Name the blood parasite species.
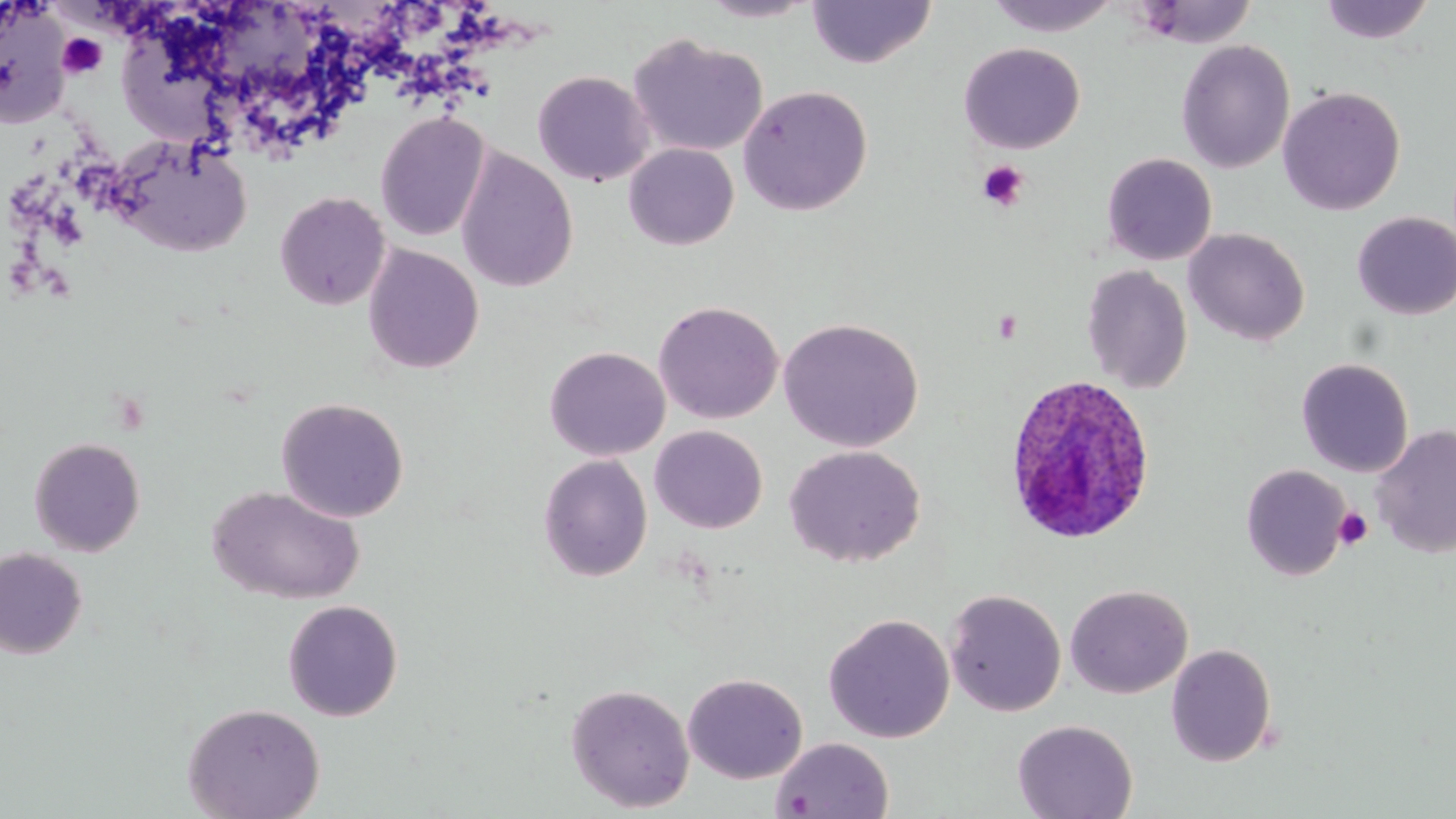
Plasmodium ovale.

Summary:
  - Coordinate format: approximate bounding boxes as (x1,y1)-(x2,y2) corner pairs in pixels
  - Plasmodium ovale-infected red blood cell locations: (1000,374)-(1155,547)
  - Platelet locations: (57,33)-(106,78), (977,160)-(1028,211), (1333,507)-(1373,550)
  - Uninfected red blood cell locations: (696,0)-(823,23), (1317,0)-(1438,45), (0,1)-(72,127), (806,1)-(937,69), (983,1)-(1123,37), (1130,1)-(1258,48), (628,33)-(768,158), (1175,40)-(1295,174), (958,42)-(1085,154), (532,70)-(654,187), (737,84)-(873,215), (1277,86)-(1406,216), (374,111)-(491,242), (106,134)-(254,257), (624,144)-(739,250), (455,147)-(578,294), (1101,153)-(1218,265), (275,191)-(391,311), (1352,212)-(1456,320), (1184,228)-(1310,346), (362,244)-(484,375), (1081,265)-(1193,393), (654,300)-(784,424), (778,317)-(924,452), (544,346)-(670,461), (1296,357)-(1414,477), (275,397)-(410,523), (649,425)-(767,533), (1371,425)-(1456,558), (28,437)-(146,556), (784,445)-(925,567), (538,454)-(653,581), (1241,463)-(1352,581), (207,485)-(365,605), (0,547)-(88,659), (1065,583)-(1193,699), (944,589)-(1067,717), (282,600)-(403,721), (822,613)-(956,743), (1166,643)-(1278,766), (682,672)-(808,784), (565,682)-(696,813), (182,702)-(325,819), (1012,718)-(1139,819), (771,736)-(894,819)
  - Preparation: thin blood smear
  - Stain: May-Grünwald-Giemsa
  - Magnification: 1000x
  - Modality: optical microscopy
  - Image size: 1456×819 pixels
  - Field of view: one of a larger specimen